Assess this cell for malaria.
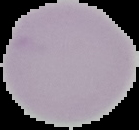

It is uninfected.

image_type: segmented cell region with the area outside set to black
image_size: 139×130 pixels
preparation: thin blood film